Assess this cell for malaria.
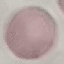
Uninfected.

Photographed with a smartphone camera at the microscope eyepiece. Thin blood film. Giemsa stain. Automatically extracted cell patch, resized to 64 × 64 pixels.